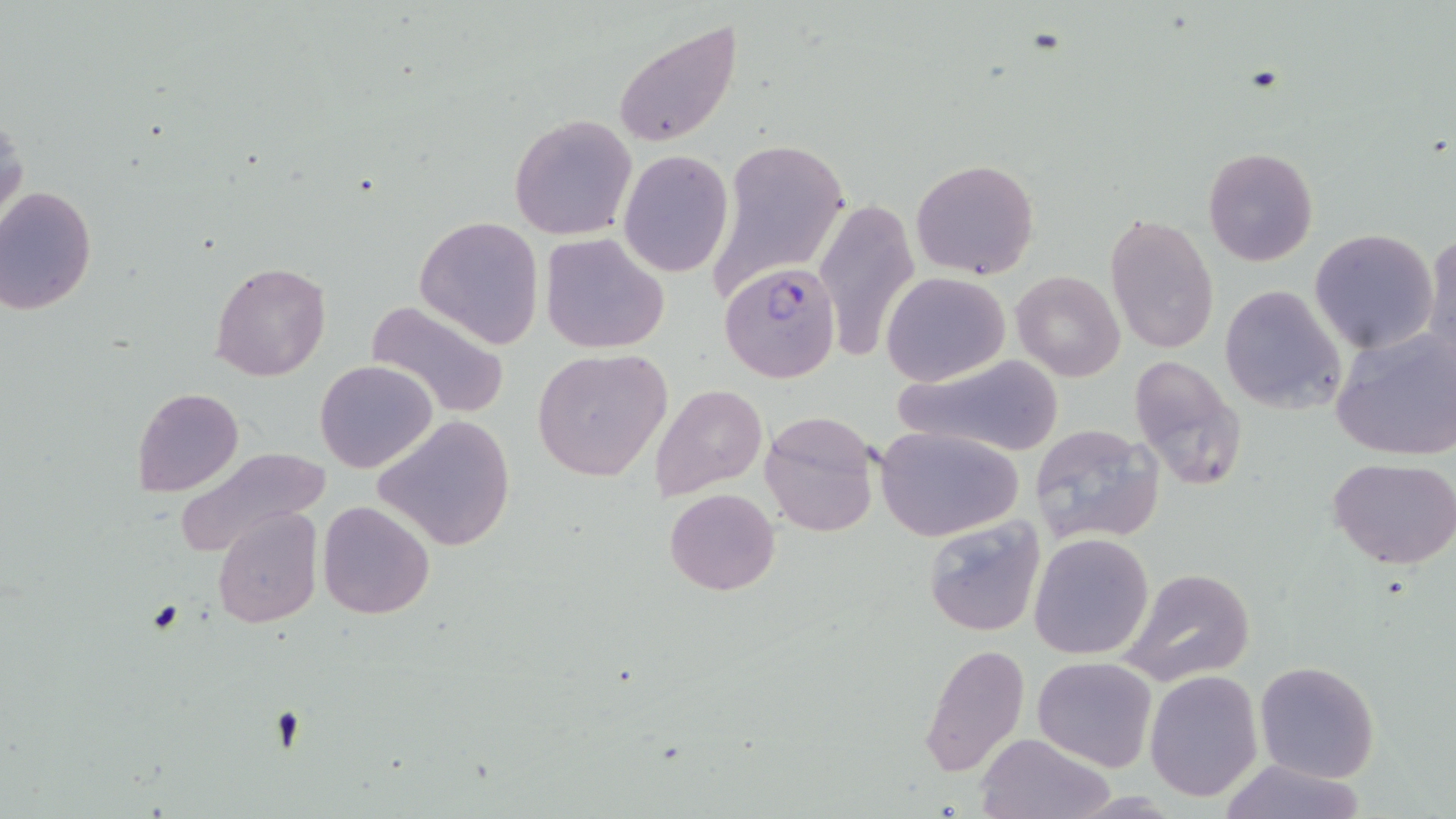

Summary:
  - Coordinate format: approximate bounding boxes as named x1/y1/x2/y2 corners in pixels
  - Plasmodium falciparum-infected red blood cell locations: (x1=718, y1=264, x2=839, y2=387)
  - Uninfected red blood cell locations: (x1=612, y1=19, x2=743, y2=148), (x1=0, y1=113, x2=26, y2=235), (x1=508, y1=114, x2=639, y2=240), (x1=704, y1=137, x2=850, y2=302), (x1=1202, y1=147, x2=1318, y2=266), (x1=619, y1=149, x2=734, y2=278), (x1=910, y1=158, x2=1040, y2=279), (x1=0, y1=186, x2=99, y2=314), (x1=813, y1=198, x2=920, y2=363), (x1=1105, y1=213, x2=1219, y2=356), (x1=414, y1=215, x2=544, y2=348), (x1=1423, y1=228, x2=1456, y2=370), (x1=1310, y1=230, x2=1438, y2=354), (x1=541, y1=233, x2=670, y2=355), (x1=209, y1=261, x2=331, y2=383), (x1=1012, y1=269, x2=1125, y2=381), (x1=881, y1=271, x2=1009, y2=387), (x1=1218, y1=285, x2=1347, y2=415), (x1=367, y1=298, x2=511, y2=421), (x1=1329, y1=326, x2=1456, y2=460), (x1=531, y1=348, x2=673, y2=482), (x1=891, y1=352, x2=1065, y2=458), (x1=1126, y1=354, x2=1245, y2=489), (x1=315, y1=358, x2=437, y2=474), (x1=650, y1=383, x2=767, y2=503), (x1=132, y1=388, x2=243, y2=497), (x1=759, y1=410, x2=884, y2=538), (x1=373, y1=414, x2=516, y2=553), (x1=1028, y1=423, x2=1166, y2=545), (x1=876, y1=425, x2=1025, y2=541), (x1=173, y1=443, x2=329, y2=559), (x1=1327, y1=457, x2=1456, y2=570), (x1=665, y1=488, x2=779, y2=594), (x1=317, y1=500, x2=435, y2=620), (x1=212, y1=508, x2=322, y2=629), (x1=921, y1=515, x2=1046, y2=637), (x1=1028, y1=532, x2=1154, y2=661), (x1=1118, y1=567, x2=1256, y2=687), (x1=918, y1=644, x2=1031, y2=777), (x1=1032, y1=657, x2=1158, y2=772), (x1=1254, y1=660, x2=1381, y2=783), (x1=1144, y1=669, x2=1263, y2=802), (x1=975, y1=732, x2=1113, y2=818), (x1=1220, y1=757, x2=1368, y2=818)
  - Slide-level diagnosis: Plasmodium falciparum
  - Field of view: single
  - Stain: May-Grünwald-Giemsa
  - Magnification: 1000x
  - Modality: optical microscopy
  - Image size: 1456×819 pixels
  - Preparation: thin blood smear